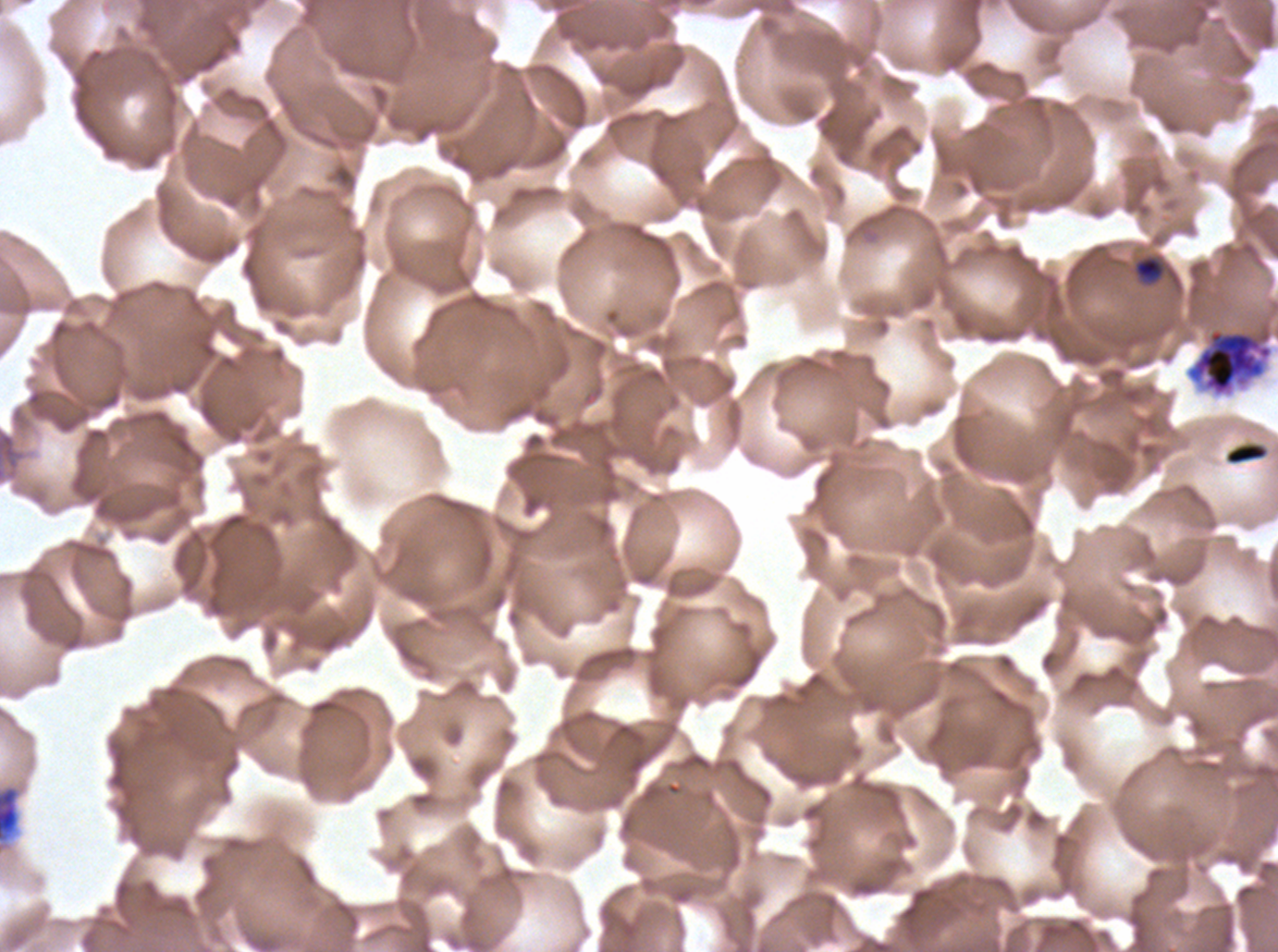 Approximate bounding boxes as [x1, y1, x2, y2] in pixels. Early schizont locations: [1186, 325, 1273, 397]. Debris locations: [1224, 442, 1268, 465], [0, 784, 21, 845]. Late-ring/early-trophozoite locations: [1133, 255, 1165, 285]. One sub-image of a larger composite. Plasmodium falciparum from a patient in The Gambia, cultured ex vivo for 24 to 48 hours. Image is 1278×952 pixels. Thin blood film. Life-cycle stages observed: late-ring/early-trophozoite, early schizont. Giemsa stain.